Locate every blood parasite and identify its species.
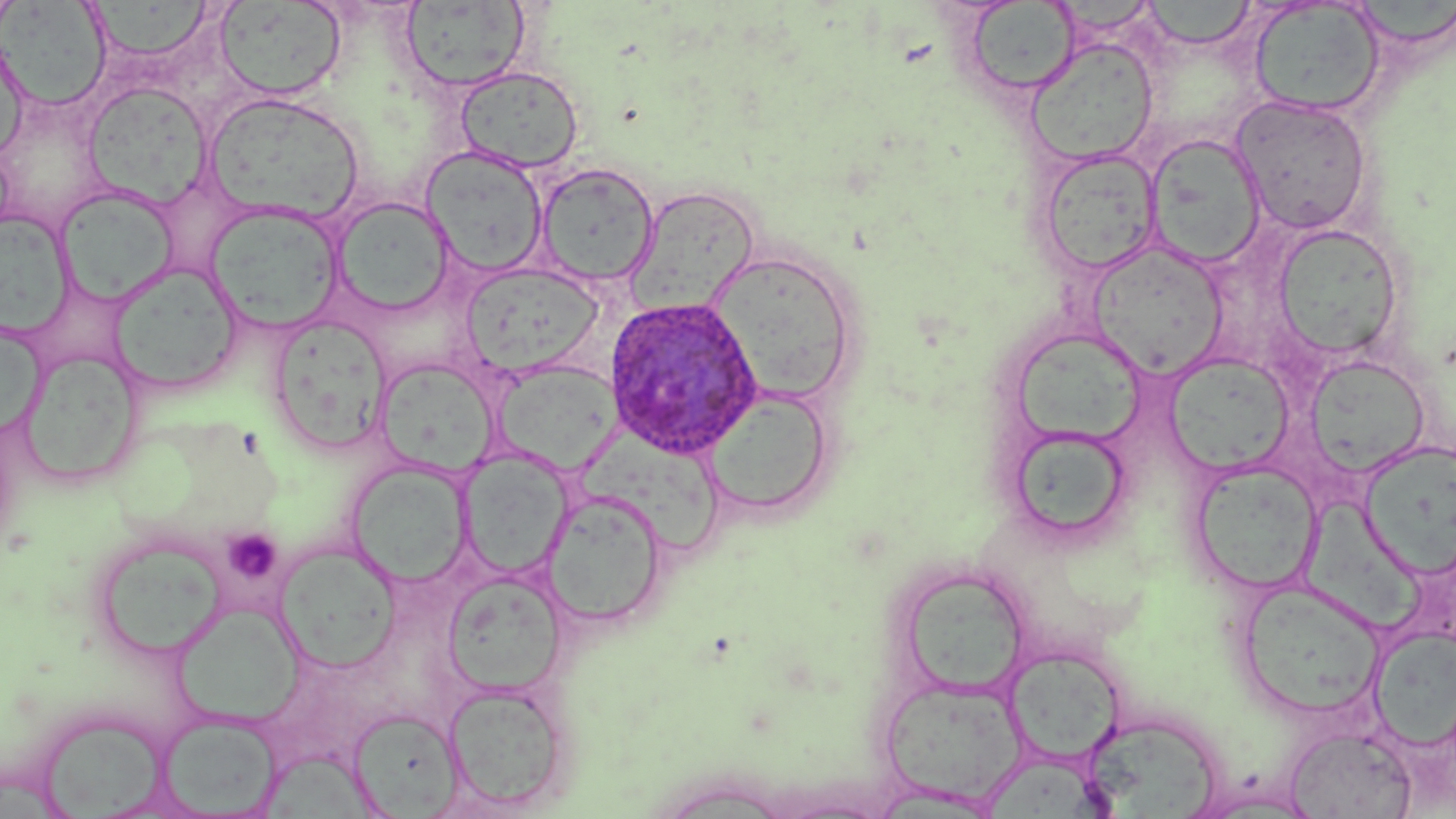
Approximate bounding boxes as named x1/y1/x2/y2 corners in pixels.
Plasmodium ovale-infected red blood cells: (x1=604, y1=294, x2=764, y2=459).
No Plasmodium falciparum, Plasmodium malariae, Plasmodium vivax, Babesia divergens, or Trypanosoma brucei observed.

Platelet locations: (x1=221, y1=527, x2=284, y2=585). Uninfected red blood cell locations: (x1=0, y1=0, x2=20, y2=39), (x1=87, y1=1, x2=218, y2=64), (x1=213, y1=1, x2=347, y2=101), (x1=400, y1=1, x2=531, y2=92), (x1=965, y1=1, x2=1079, y2=94), (x1=1141, y1=1, x2=1259, y2=49), (x1=1249, y1=2, x2=1384, y2=116), (x1=1358, y1=2, x2=1456, y2=46), (x1=1, y1=3, x2=112, y2=111), (x1=0, y1=30, x2=29, y2=165), (x1=1027, y1=39, x2=1158, y2=165), (x1=454, y1=65, x2=584, y2=174), (x1=83, y1=82, x2=211, y2=208), (x1=204, y1=91, x2=365, y2=225), (x1=1230, y1=94, x2=1374, y2=235), (x1=1146, y1=132, x2=1268, y2=269), (x1=420, y1=145, x2=550, y2=277), (x1=1037, y1=147, x2=1162, y2=276), (x1=535, y1=162, x2=660, y2=287), (x1=626, y1=185, x2=760, y2=319), (x1=56, y1=186, x2=179, y2=306), (x1=332, y1=196, x2=456, y2=317), (x1=206, y1=202, x2=344, y2=333), (x1=0, y1=210, x2=73, y2=337), (x1=1272, y1=223, x2=1407, y2=361), (x1=1087, y1=240, x2=1229, y2=375), (x1=708, y1=251, x2=860, y2=404), (x1=108, y1=261, x2=244, y2=395), (x1=462, y1=262, x2=603, y2=378), (x1=268, y1=314, x2=392, y2=453), (x1=0, y1=320, x2=46, y2=439), (x1=1012, y1=330, x2=1150, y2=446), (x1=20, y1=348, x2=143, y2=487), (x1=1163, y1=352, x2=1294, y2=476), (x1=1304, y1=354, x2=1431, y2=479), (x1=494, y1=360, x2=619, y2=474), (x1=374, y1=361, x2=503, y2=479), (x1=703, y1=389, x2=833, y2=520), (x1=1005, y1=424, x2=1134, y2=545), (x1=576, y1=434, x2=725, y2=552), (x1=1357, y1=442, x2=1456, y2=582), (x1=459, y1=450, x2=574, y2=579), (x1=1189, y1=459, x2=1322, y2=594), (x1=348, y1=460, x2=473, y2=588), (x1=542, y1=489, x2=668, y2=630), (x1=1300, y1=495, x2=1432, y2=633), (x1=91, y1=531, x2=229, y2=664), (x1=273, y1=542, x2=401, y2=673), (x1=442, y1=570, x2=566, y2=694), (x1=909, y1=572, x2=1024, y2=694), (x1=1237, y1=579, x2=1385, y2=721), (x1=173, y1=601, x2=304, y2=727), (x1=1370, y1=628, x2=1456, y2=750), (x1=1006, y1=644, x2=1127, y2=766), (x1=879, y1=676, x2=1027, y2=804), (x1=442, y1=681, x2=572, y2=812), (x1=347, y1=707, x2=464, y2=816), (x1=156, y1=713, x2=283, y2=817), (x1=36, y1=714, x2=172, y2=814), (x1=1090, y1=725, x2=1221, y2=819), (x1=1285, y1=726, x2=1416, y2=818), (x1=256, y1=746, x2=379, y2=819), (x1=985, y1=761, x2=1097, y2=819), (x1=1185, y1=788, x2=1324, y2=818). Slide-level diagnosis: Plasmodium ovale. Image is 1456×819 pixels. Optical microscopy. Thin blood smear. 1000x magnification. May-Grünwald-Giemsa stain. One field of a larger specimen.